Assess this cell for malaria.
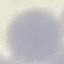

It is uninfected.

Giemsa-stained preparation. Acquired by smartphone through the microscope eyepiece. Automatically extracted cell patch, resized to 64 × 64 pixels. Thin blood smear.